Outline each uninfected red blood cell.
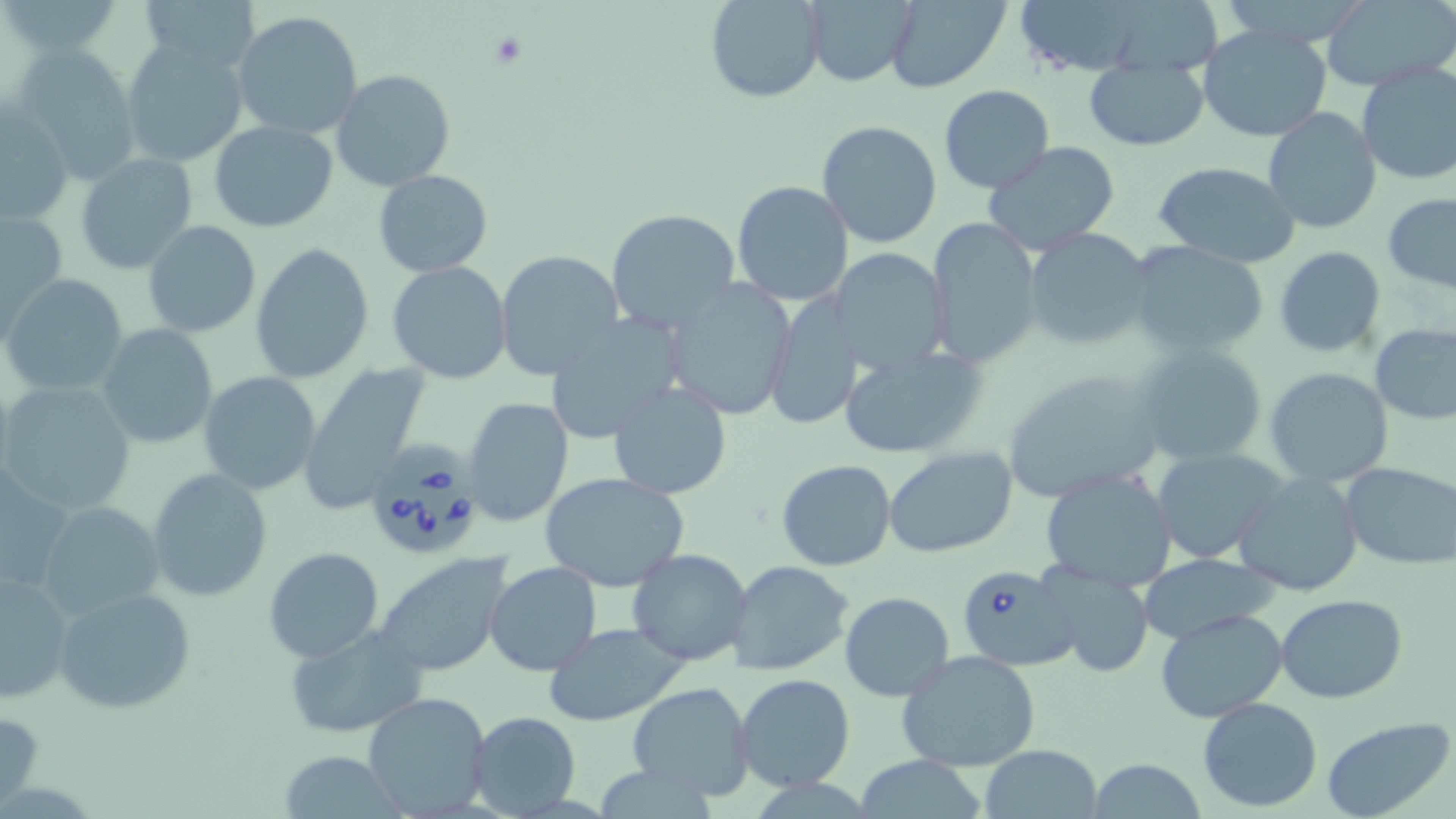
Approximate bounding boxes as (x1,y1)-(x2,y2) corner pairs in pixels.
Uninfected red blood cells: (139,0)-(260,73), (704,0)-(826,103), (885,0)-(1010,93), (1012,0)-(1156,75), (1323,0)-(1456,89), (803,1)-(916,87), (231,11)-(364,139), (1198,26)-(1332,144), (120,38)-(250,168), (12,45)-(142,182), (1085,57)-(1208,153), (1355,64)-(1456,186), (333,69)-(454,191), (938,85)-(1054,193), (1,103)-(74,226), (1262,108)-(1382,232), (210,120)-(338,232), (815,120)-(944,249), (983,142)-(1121,253), (75,153)-(199,275), (1153,162)-(1301,268), (373,170)-(492,276), (731,180)-(855,305), (1383,193)-(1456,291), (1,208)-(68,332), (607,208)-(743,335), (925,217)-(1044,371), (143,219)-(261,339), (1023,229)-(1153,351), (251,243)-(375,383), (1128,243)-(1272,358), (1274,246)-(1387,357), (829,248)-(952,375), (494,249)-(623,378), (386,261)-(513,385), (4,275)-(130,397), (662,278)-(797,421), (765,293)-(868,429), (543,316)-(683,443), (98,324)-(218,449), (1370,325)-(1456,423), (836,342)-(991,459), (1130,343)-(1268,466), (297,362)-(429,510), (1265,366)-(1394,488), (1000,367)-(1166,502), (197,371)-(322,495), (609,379)-(731,500), (2,381)-(136,514), (462,396)-(573,525), (882,446)-(1019,559), (1153,448)-(1284,564), (775,460)-(896,571), (1340,464)-(1456,568), (1040,468)-(1180,592), (147,469)-(272,601), (0,470)-(76,595), (541,472)-(690,591), (1233,472)-(1365,596), (40,500)-(166,621), (262,546)-(384,664), (625,548)-(754,666), (1137,552)-(1281,647), (374,554)-(514,677), (726,560)-(854,676), (484,562)-(601,676), (1041,565)-(1154,677), (0,570)-(75,704), (53,588)-(196,714), (839,592)-(953,701), (1277,595)-(1407,704), (1156,608)-(1288,721), (544,621)-(689,725), (283,624)-(427,740), (898,651)-(1041,773), (733,673)-(856,791), (627,682)-(756,802), (361,690)-(493,816), (1195,696)-(1323,812), (0,704)-(44,811), (468,711)-(579,817), (1321,718)-(1453,819), (979,744)-(1104,819), (280,750)-(401,817), (852,756)-(992,817), (1089,758)-(1206,818).

Summary:
  - Platelet locations: (485,30)-(531,70)
  - Babesia divergens-infected red blood cell locations: (364,445)-(481,560), (954,562)-(1078,672)
  - Slide-level diagnosis: Babesia divergens
  - Modality: optical microscopy
  - Preparation: thin blood smear
  - Image size: 1456×819 pixels
  - Field of view: single
  - Stain: May-Grünwald-Giemsa
  - Magnification: 1000x